Point out each malaria parasite.
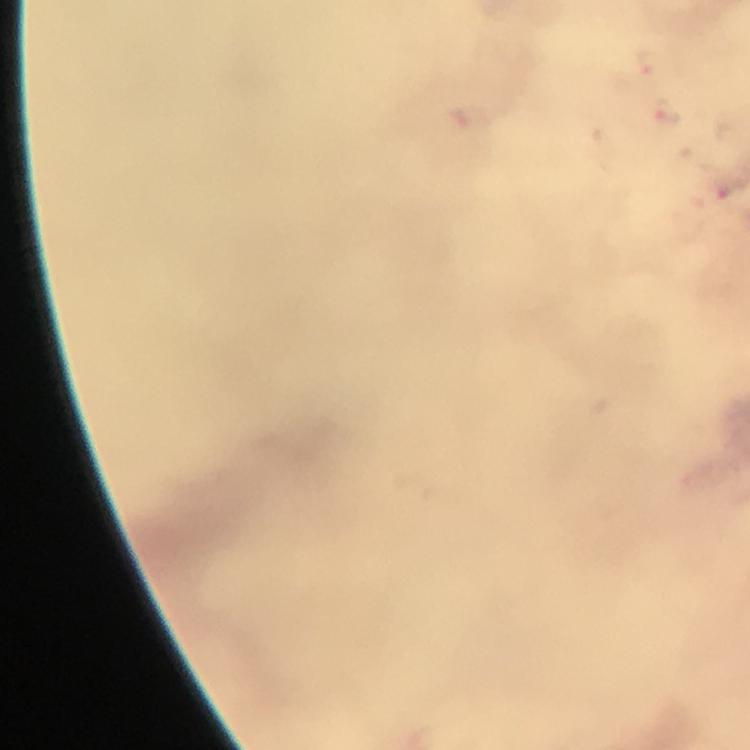
Approximate centers as [x, y] in pixels.
Malaria parasites: [648, 60], [670, 113], [718, 190].

From a malaria diagnostic workup. Giemsa stain. At 100x magnification. Immersion oil was used. A crop from one field of view. Image is 750×750 pixels. Thick blood smear. Photographed with a smartphone mounted on the microscope.